Assess this cell for malaria.
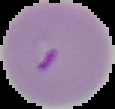

It is parasitized.

From a thin blood film. The area outside the segmented cell region is set to black. Image is 115×109 pixels.